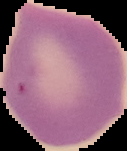

Result: no malaria parasites seen. From a thin blood smear. Segmented cell region on a black background. Image is 127×151 pixels.